Give the preparation type.
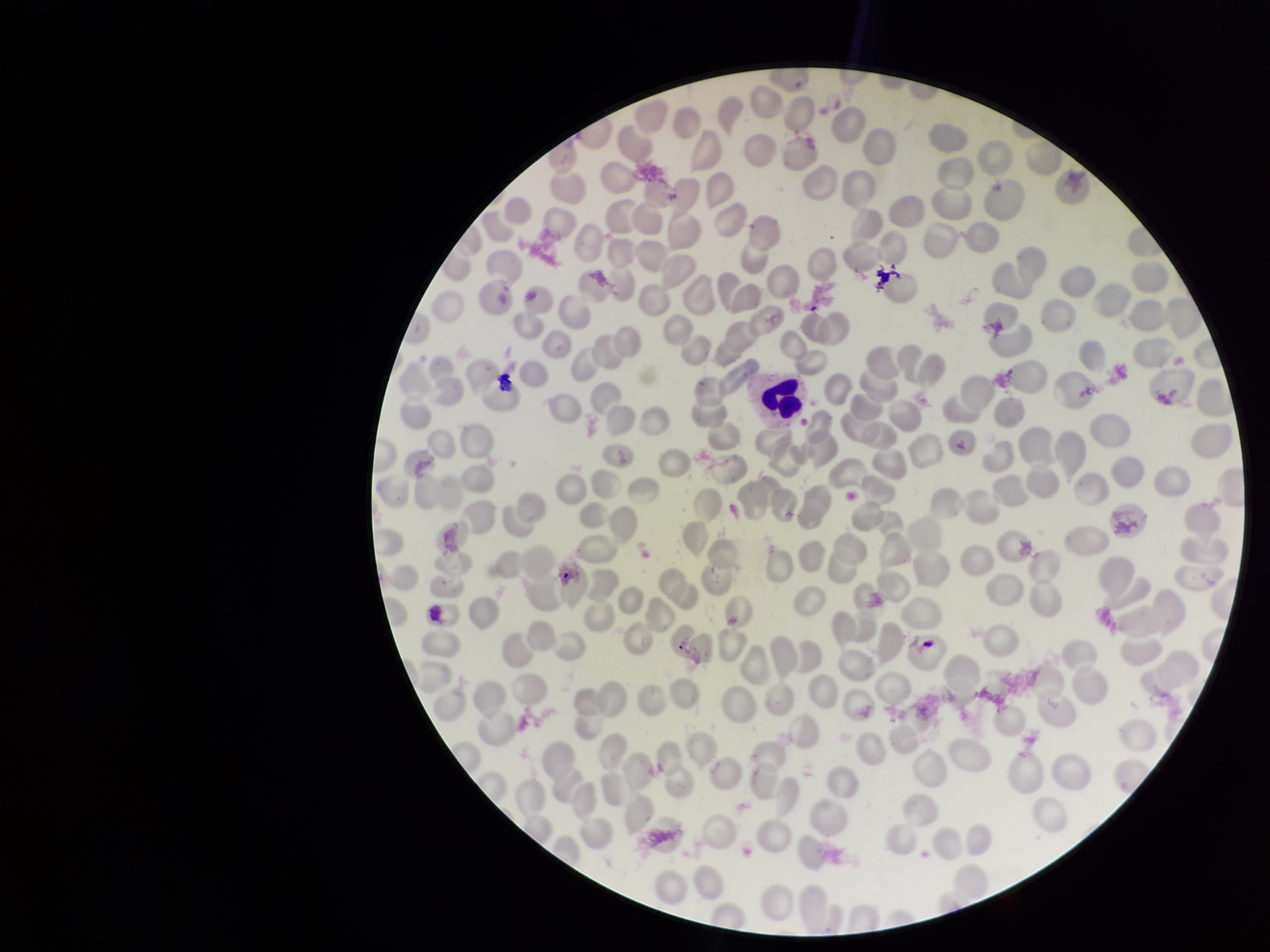
It is a thin blood smear.

Summary:
  - Capture: smartphone photograph through the microscope eyepiece
  - Field of view: one from this slide
  - Red blood cell count: 277
  - Image size: 1270×952 pixels
  - Stain: Giemsa
  - Species reported for this patient: Plasmodium vivax
  - Parasitized red blood cells: none detected
  - Parasitized red blood cell count: 0
  - Patient malaria status: infected